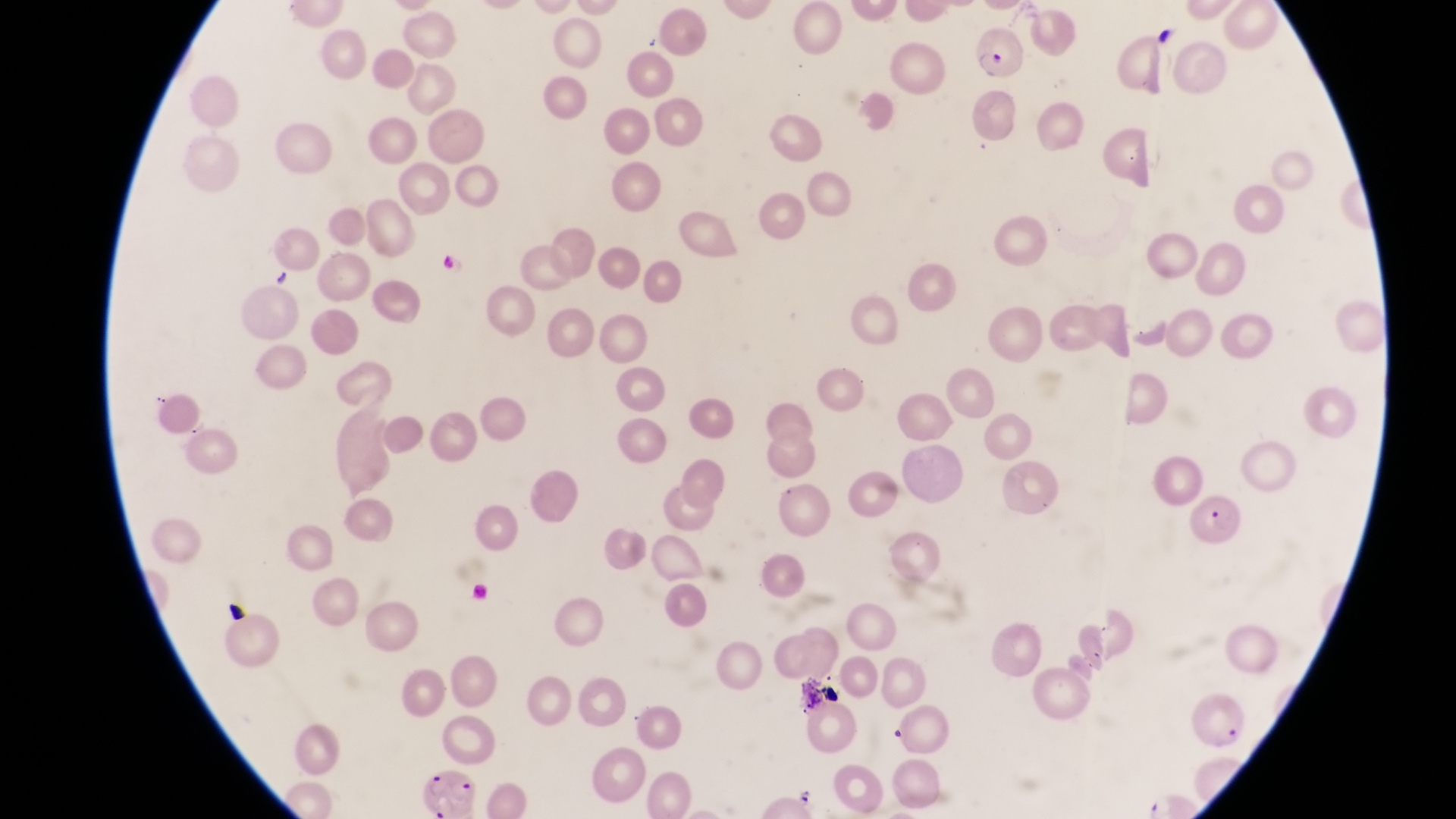
Approximate bounding boxes as {left, top, right, bottom} in pixels. Artifact (platelet-like body, stain precipitate, or debris) locations: {1153, 19, 1179, 49}, {431, 245, 460, 274}, {270, 262, 296, 292}, {222, 595, 244, 615}, {802, 676, 842, 713}. Parasitised red blood cell locations: {967, 33, 1026, 82}, {1189, 488, 1249, 554}, {413, 763, 492, 816}. One field of view. Magnification of 1000x. Collected in Uganda. Image is 1456×819 pixels. Photographed through the eyepiece of an Olympus CX-23 microscope with a smartphone camera. Thin blood smear.